Identify the parasite.
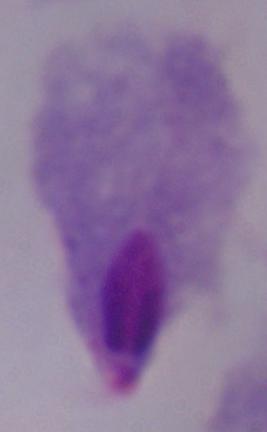

A trichomonad.

1000x magnification. Photomicrograph.